Describe the morphology of the red blood cells.
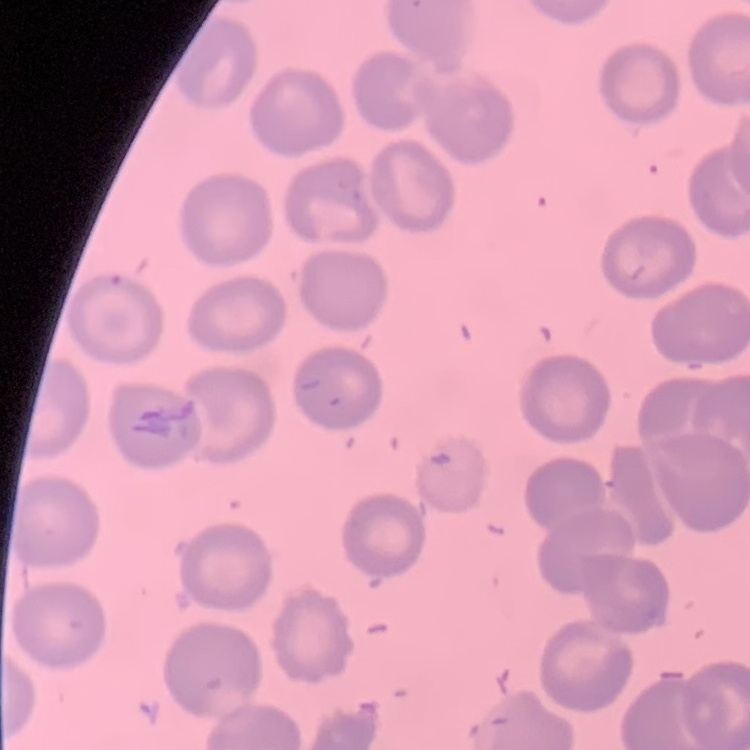
No rouleaux formation.

preparation = thin blood smear
image type = one tile cut from a larger photomicrograph
stain = Field's or Giemsa